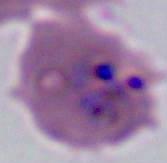

A Plasmodium parasite is seen. Captured at either 400x or 1000x magnification. Micrograph.